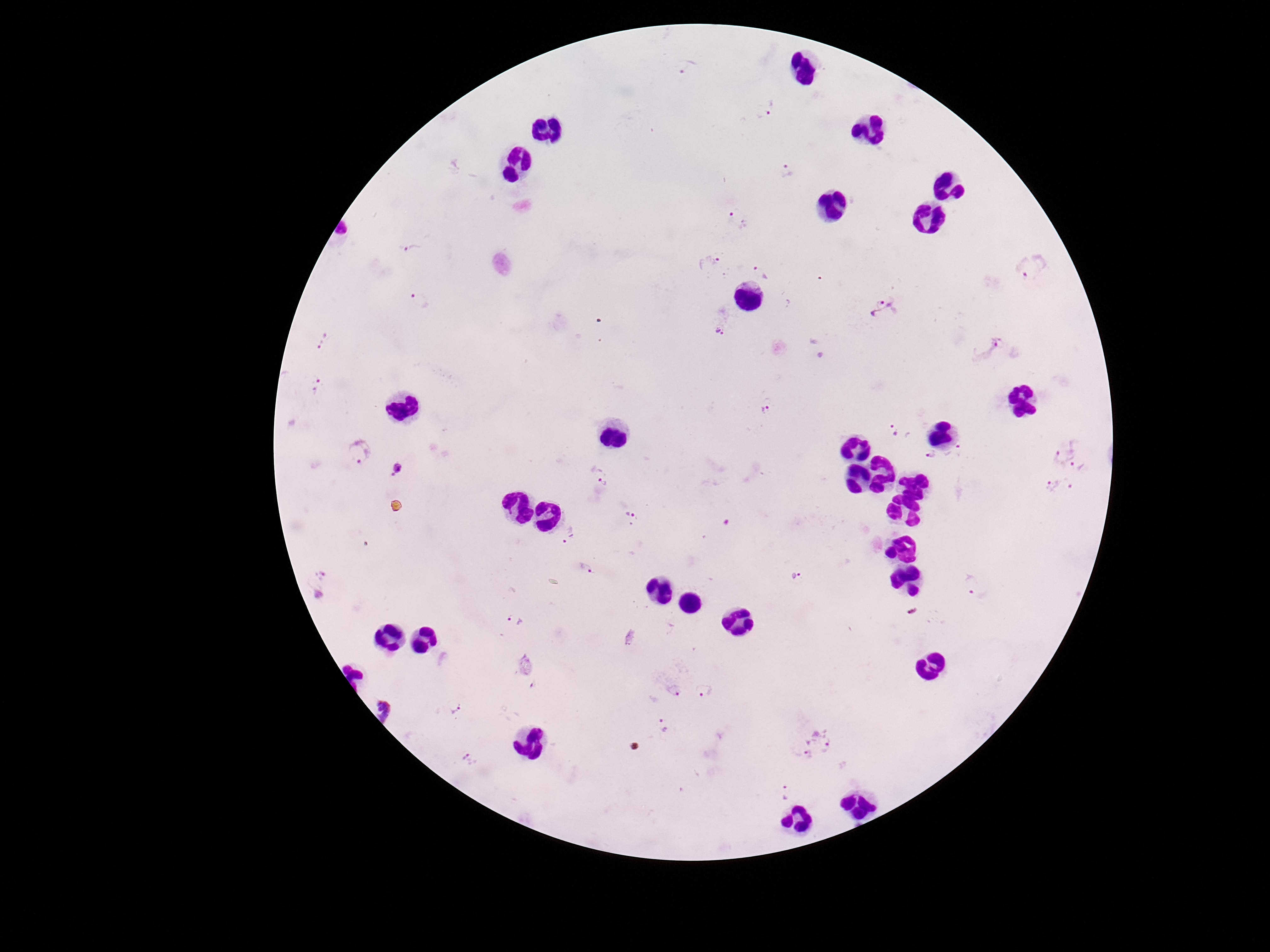 Approximate object centers, in pixels from the top-left corner. Plasmodium parasite locations: (x=687, y=67), (x=766, y=108), (x=787, y=171), (x=739, y=219), (x=411, y=250), (x=710, y=260), (x=1030, y=269), (x=760, y=272), (x=419, y=301), (x=886, y=309), (x=719, y=331), (x=323, y=342), (x=988, y=346), (x=315, y=386), (x=764, y=409), (x=894, y=432), (x=1061, y=450), (x=359, y=451), (x=955, y=451), (x=931, y=454), (x=1077, y=464), (x=398, y=470), (x=599, y=474), (x=1071, y=482), (x=1051, y=485), (x=631, y=516), (x=568, y=535), (x=586, y=568), (x=797, y=577), (x=318, y=581), (x=975, y=586), (x=515, y=621), (x=535, y=685), (x=705, y=689), (x=673, y=692), (x=455, y=707), (x=386, y=712), (x=663, y=724), (x=823, y=739), (x=808, y=758), (x=468, y=760), (x=784, y=792). Giemsa stain. Patient malaria status: infected. Image is 1270×952 pixels. Smartphone photograph taken through the microscope eyepiece. One field from this slide. Thick blood film. 100x magnification.